Locate leukocytes (white blood cells).
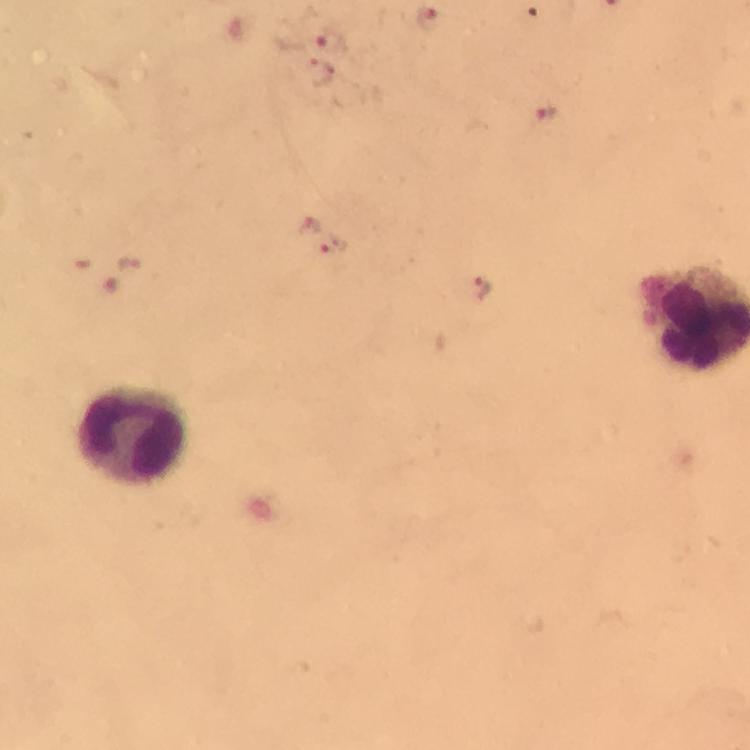

Approximate object centers, in pixels from the top-left corner.
Leukocytes: (x=132, y=435).

Plasmodium parasite locations = approximate object centers, in pixels from the top-left corner: (x=429, y=20), (x=332, y=43), (x=321, y=74), (x=542, y=114), (x=308, y=226), (x=332, y=244), (x=133, y=266), (x=481, y=288)
stain = Giemsa
magnification = 100x
capture = smartphone mounted on the microscope
cropped from = a single field of view
context = from a malaria diagnostic workup
preparation = thick smear
image size = 750×750 pixels
immersion oil = used